Classify this cell by malaria status.
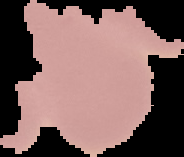

Uninfected.

Cell region segmented out of the field of view; the surrounding area is masked to black. From a thin blood film. Image is 184×157 pixels.